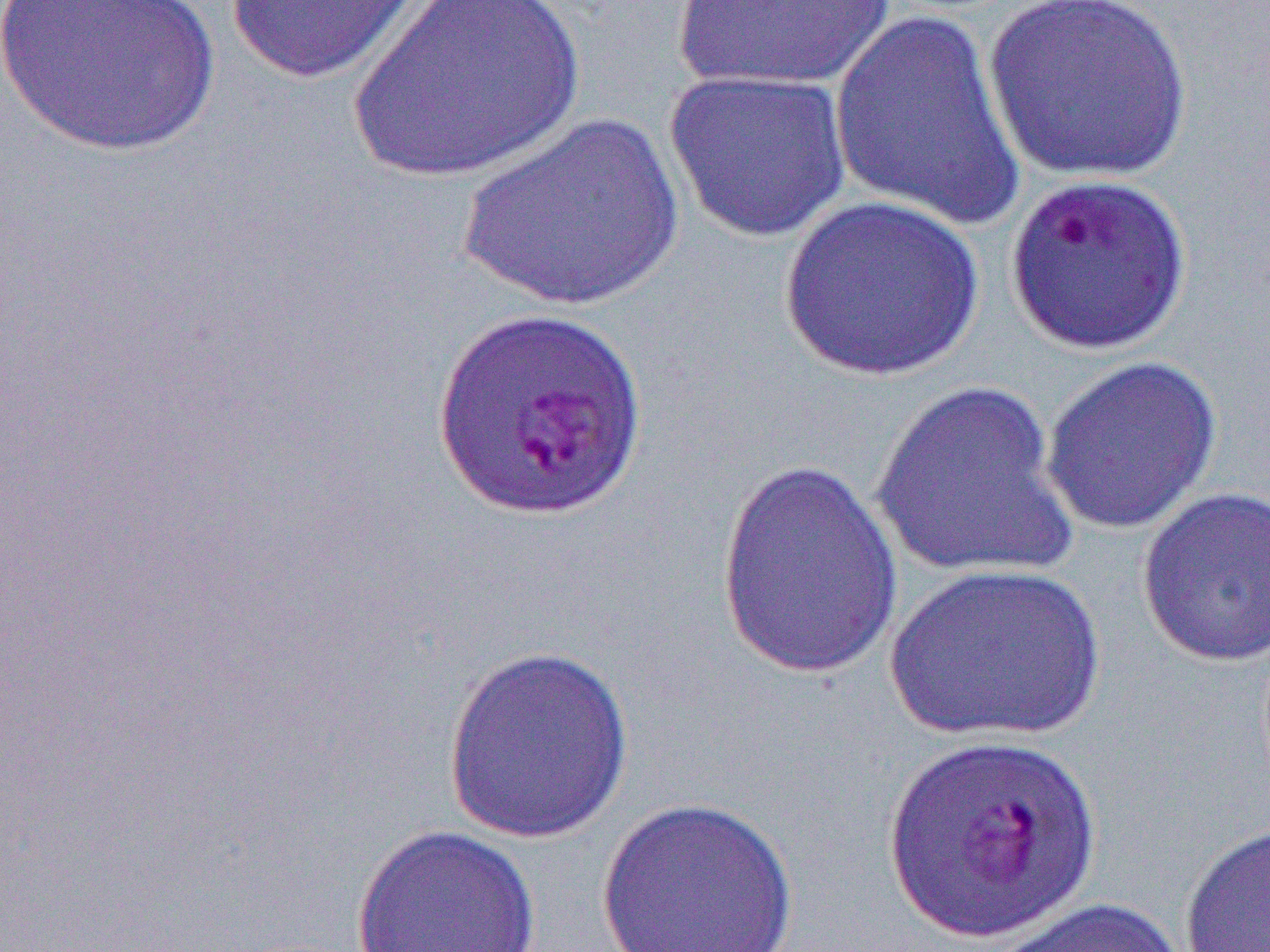

Summary:
  - Coordinate format: approximate bounding boxes as (x1,y1)-(x2,y2) corner pairs in pixels
  - Uninfected red blood cell locations: (0,0)-(222,157), (346,0)-(585,184), (671,0)-(899,95), (984,0)-(1194,184), (222,1)-(435,84), (828,10)-(1029,233), (664,69)-(853,243), (457,114)-(685,313), (1004,171)-(1194,357), (779,194)-(984,382), (1039,354)-(1223,537), (868,380)-(1081,584), (715,457)-(906,682), (1136,486)-(1269,668), (883,562)-(1107,744), (441,644)-(635,843), (594,796)-(800,952), (1179,820)-(1270,952), (350,824)-(541,952), (982,895)-(1193,952)
  - Slide-level diagnosis: Plasmodium falciparum
  - Magnification: 1000x
  - Modality: optical microscopy
  - Image size: 1270×952 pixels
  - Preparation: thin blood film
  - Field of view: one of a larger specimen